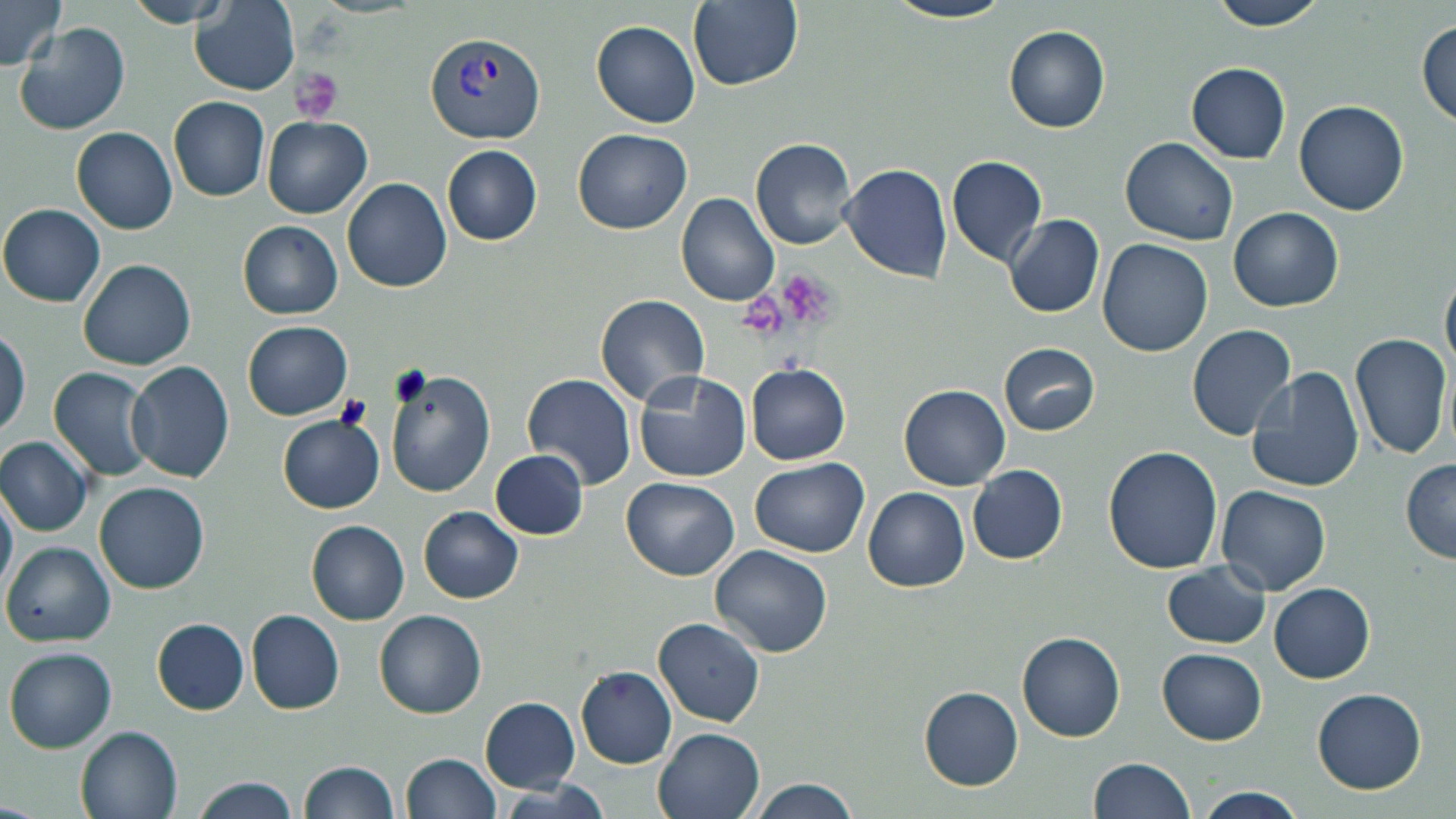

Approximate bounding boxes as (x1, y1, x2, y2) in pixels. Platelet locations: (291, 68, 343, 124), (778, 268, 842, 331). Uninfected red blood cell locations: (118, 0, 238, 26), (689, 0, 802, 90), (884, 0, 1015, 26), (1204, 0, 1330, 30), (1, 1, 66, 71), (191, 1, 300, 98), (1417, 19, 1455, 126), (591, 20, 701, 127), (14, 22, 131, 135), (1004, 26, 1111, 132), (1185, 61, 1292, 163), (169, 96, 271, 200), (1294, 100, 1409, 216), (262, 116, 372, 216), (269, 124, 434, 263), (71, 126, 179, 235), (572, 128, 692, 234), (749, 137, 858, 250), (1120, 138, 1238, 246), (443, 145, 541, 245), (947, 154, 1047, 266), (839, 162, 952, 282), (342, 177, 453, 292), (677, 193, 781, 307), (0, 203, 106, 306), (1228, 207, 1344, 312), (1005, 215, 1104, 318), (239, 222, 344, 319), (1097, 236, 1213, 356), (79, 257, 197, 370), (1442, 270, 1456, 375), (595, 293, 712, 407), (243, 321, 353, 419), (1186, 323, 1297, 441), (0, 330, 27, 437), (1349, 333, 1452, 462), (999, 343, 1098, 435), (127, 360, 236, 483), (748, 365, 852, 465), (1245, 365, 1366, 495), (49, 366, 154, 482), (385, 368, 496, 496), (634, 371, 752, 482), (523, 372, 638, 491), (901, 386, 1009, 490), (277, 416, 385, 513), (0, 435, 94, 535), (1102, 445, 1223, 574), (491, 450, 589, 540), (751, 457, 869, 556), (1400, 459, 1456, 562), (967, 464, 1067, 563), (623, 477, 740, 578), (0, 481, 16, 602), (95, 482, 208, 594), (1219, 486, 1331, 596), (863, 487, 970, 592), (419, 507, 523, 603), (307, 519, 410, 624), (4, 542, 115, 645), (711, 545, 831, 657), (1162, 561, 1271, 648), (1268, 583, 1374, 682), (246, 610, 346, 713), (375, 610, 487, 719), (654, 617, 766, 726), (153, 619, 248, 714), (1017, 631, 1126, 742), (1156, 647, 1267, 744), (5, 648, 117, 754), (576, 666, 677, 768), (920, 688, 1023, 790), (1314, 689, 1427, 792), (481, 696, 581, 791), (77, 726, 183, 819), (654, 726, 765, 819), (403, 753, 500, 819), (1087, 756, 1197, 819), (299, 759, 400, 819), (190, 777, 302, 819), (744, 777, 862, 819), (500, 782, 611, 818), (1198, 787, 1305, 818). Plasmodium vivax-infected red blood cell locations: (423, 32, 545, 145). Slide-level diagnosis: Plasmodium vivax. May-Grünwald-Giemsa-stained preparation. Optical microscopy. One field of a larger specimen. Captured at 1000x magnification. Thin blood film. Image is 1456×819 pixels.